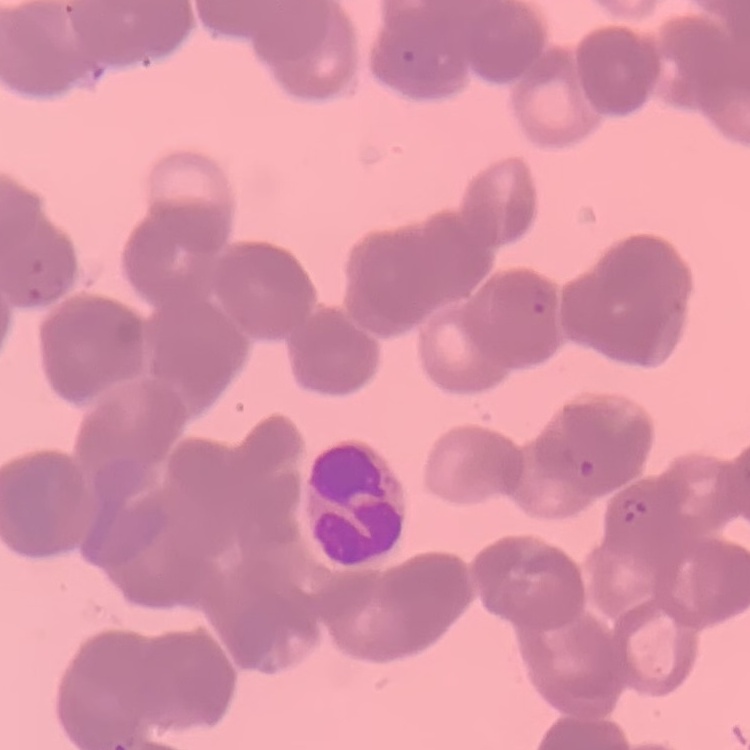
Summary:
  - Erythrocyte morphology: rouleaux formation
  - Preparation: thin blood film
  - Image type: square crop of a larger photomicrograph
  - Stain: Field's or Giemsa